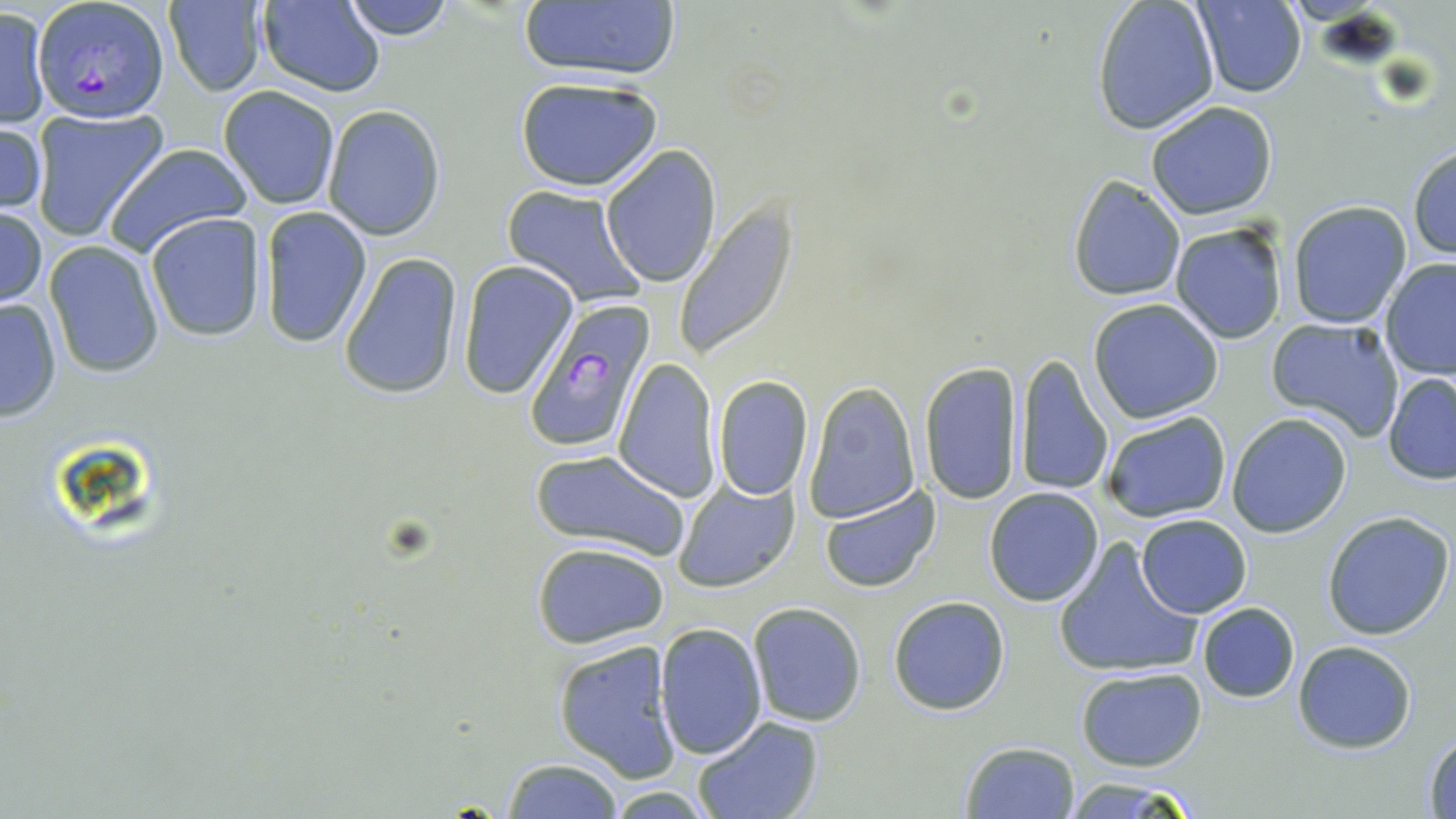 Approximate bounding boxes as (x1,y1)-(x2,y2) corner pairs in pixels. Plasmodium falciparum-infected red blood cell locations: (34,1)-(167,124), (520,298)-(659,453). Uninfected red blood cell locations: (338,0)-(459,40), (1091,0)-(1221,135), (257,1)-(385,96), (1193,1)-(1306,98), (164,2)-(268,96), (515,3)-(684,83), (1,7)-(50,128), (514,75)-(663,193), (219,85)-(341,210), (1146,100)-(1278,220), (322,106)-(445,241), (29,109)-(169,242), (0,118)-(47,220), (1408,142)-(1456,263), (101,143)-(253,261), (601,144)-(722,289), (1065,173)-(1186,301), (501,187)-(647,308), (1288,201)-(1413,328), (674,203)-(800,358), (1,204)-(48,309), (258,207)-(372,348), (145,214)-(267,342), (1169,220)-(1289,346), (43,241)-(166,378), (338,252)-(465,400), (1381,258)-(1456,381), (456,259)-(578,399), (1,296)-(63,421), (1088,299)-(1224,422), (1266,317)-(1405,439), (1015,353)-(1114,498), (612,357)-(720,501), (920,359)-(1025,506), (1383,372)-(1456,484), (711,375)-(814,502), (805,382)-(920,523), (1101,412)-(1231,523), (1226,413)-(1353,538), (530,447)-(694,564), (673,477)-(800,593), (820,486)-(941,593), (984,486)-(1105,606), (1323,512)-(1454,641), (1136,513)-(1251,619), (1052,537)-(1204,682), (531,541)-(669,648), (888,596)-(1009,715), (748,601)-(868,726), (1198,602)-(1300,703), (655,623)-(768,761), (553,639)-(682,782), (1292,640)-(1417,753), (1076,667)-(1207,770), (691,716)-(825,819), (1423,733)-(1456,817), (957,740)-(1081,818), (500,757)-(625,819), (1059,775)-(1204,818), (603,786)-(718,817). Slide-level diagnosis: Plasmodium falciparum. Single field of view. May-Grünwald-Giemsa stain. Thin blood smear. Image is 1456×819 pixels. Light microscopy. Captured at 1000x magnification.